State which cell type is depicted.
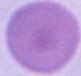
This is an erythrocyte.

magnification = 1000x
modality = micrograph